Report the malaria status of this cell.
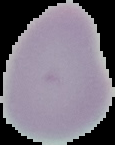

Uninfected.

The area outside the segmented cell region is set to black. Image is 115×145 pixels. From a thin blood smear.